Evaluate for parasitized red blood cells.
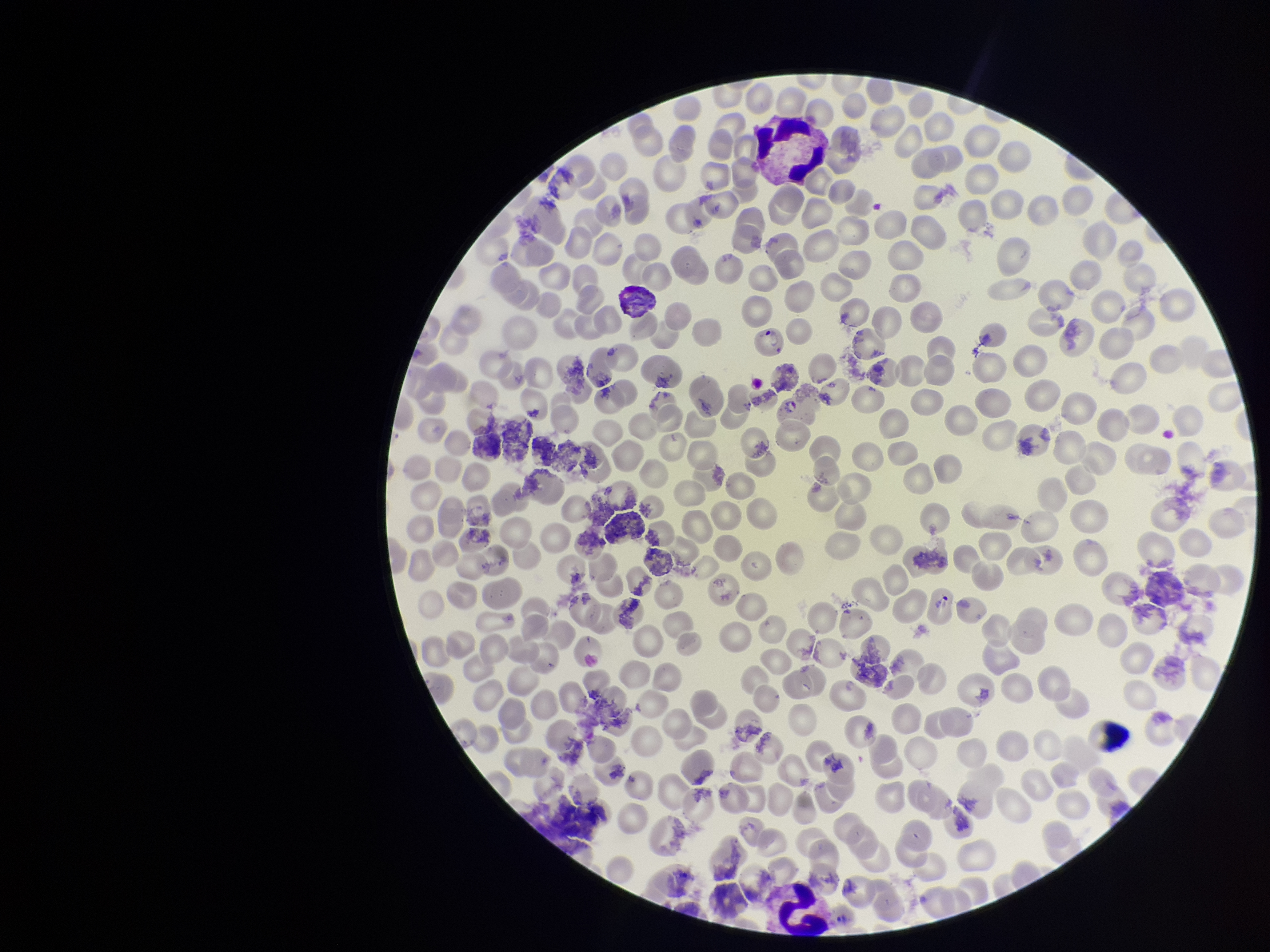

None detected.

species reported for this patient = Plasmodium vivax
field of view = single
red blood cell count = 208
stain = Giemsa
capture = smartphone photograph through the microscope eyepiece
parasitized red blood cell count = 0
preparation = thin smear
image size = 1270×952 pixels
patient malaria status = positive